Locate every Plasmodium parasite.
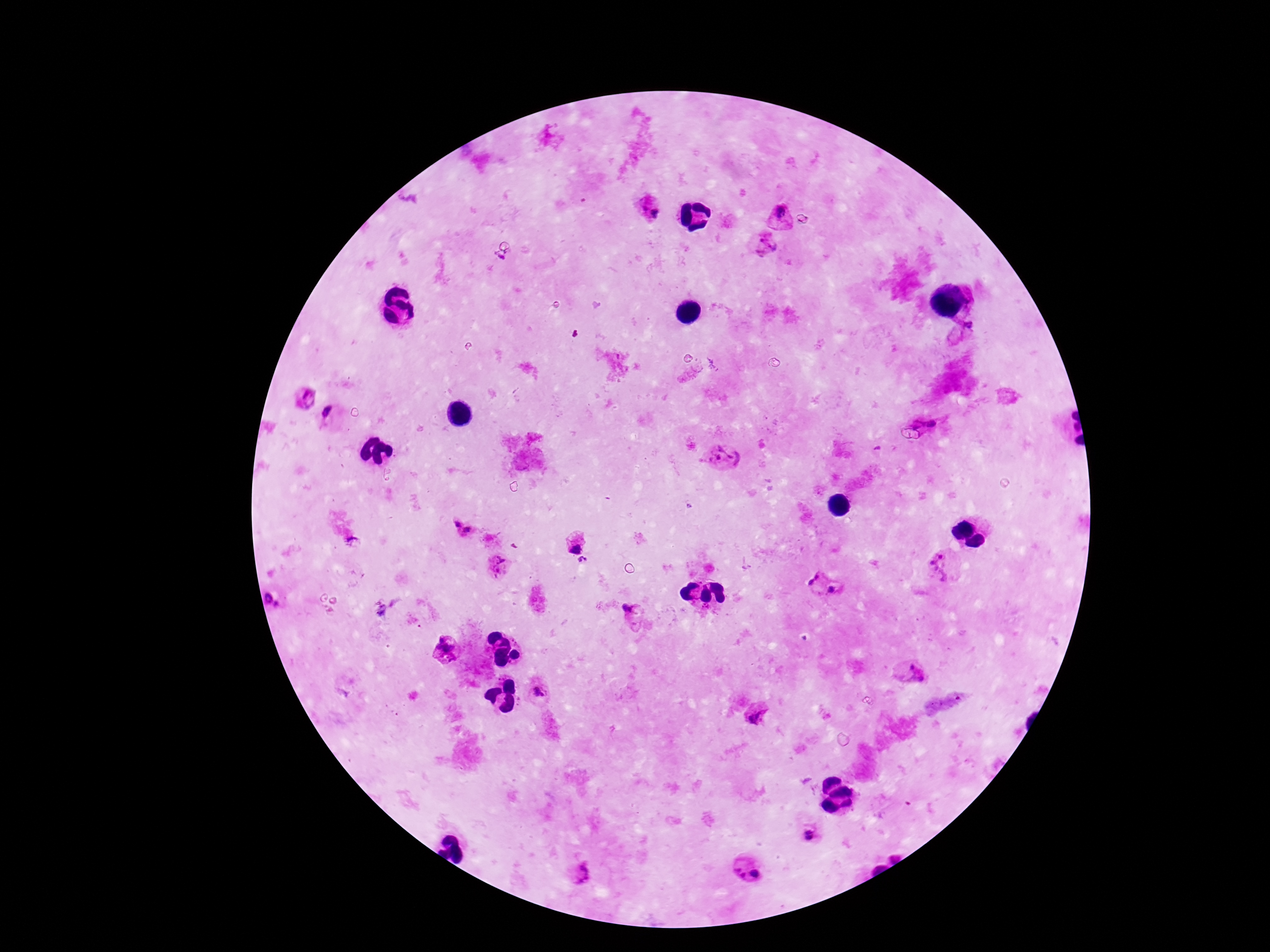
Approximate centers as (x, y) in pixels.
Plasmodium parasites: (649, 211), (778, 214), (767, 245), (965, 326), (306, 399), (332, 415), (930, 420), (724, 457), (457, 524), (467, 530), (575, 547), (583, 562), (501, 564), (941, 567), (815, 580), (833, 590), (273, 600), (630, 607), (446, 645), (911, 672), (536, 692), (758, 716), (810, 834), (579, 873), (739, 873), (755, 873).

{
  "stain": "Giemsa",
  "patient_malaria_status": "positive",
  "preparation": "thick peripheral-blood smear",
  "field_of_view": "one from this slide",
  "magnification": "100x",
  "image_size": "1270×952 pixels",
  "capture": "smartphone camera through the microscope eyepiece"
}